Report the malaria status of this cell.
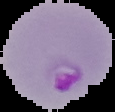

It is parasitized.

From a thin blood film. Image is 115×112 pixels. Segmented cell region on a black background.